Locate and identify every blood parasite.
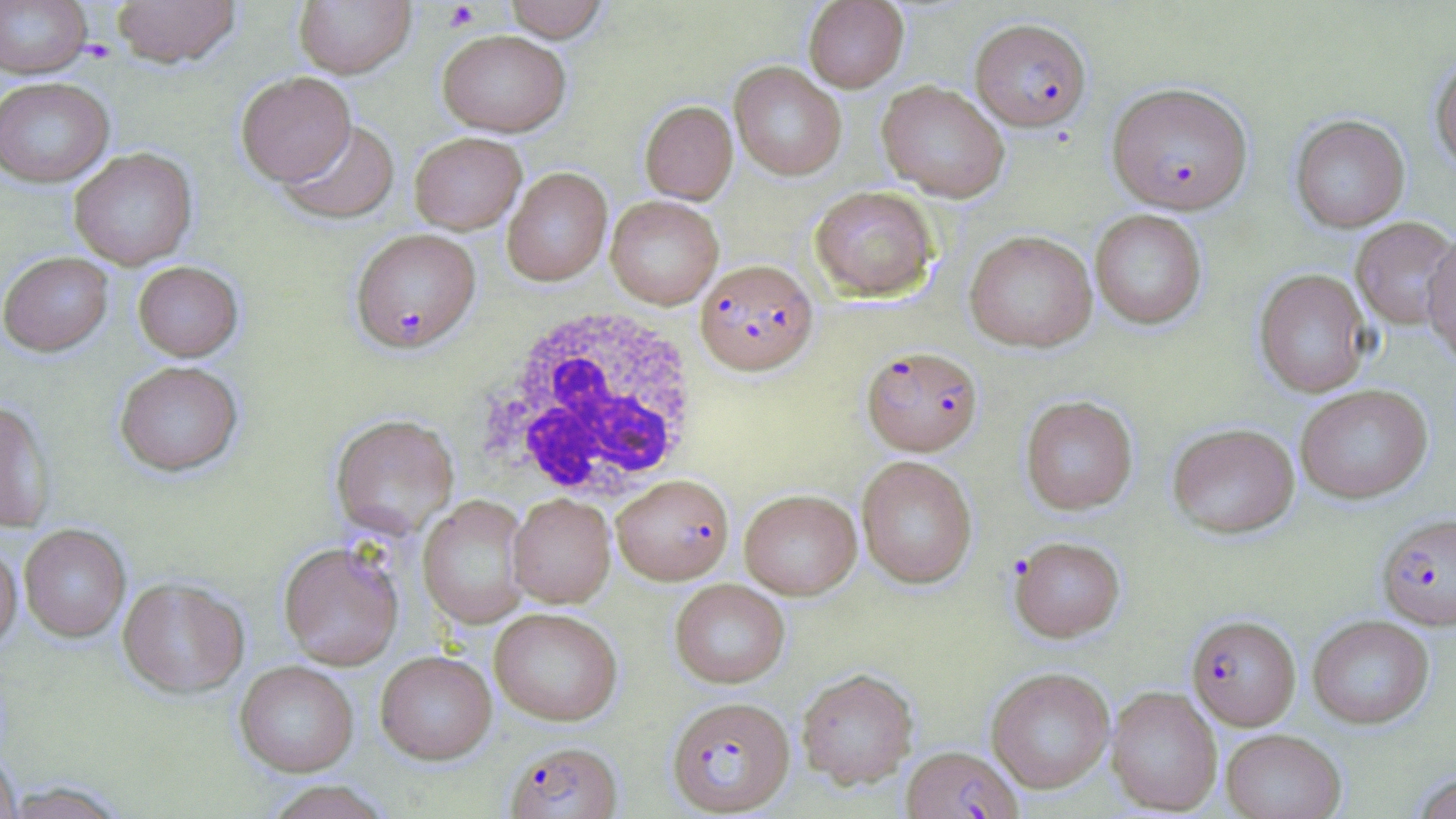
Approximate bounding boxes as (x1, y1, x2, y2) in pixels.
Plasmodium falciparum-infected red blood cells (subset): (970, 18, 1091, 132), (1107, 81, 1253, 215), (350, 228, 481, 353), (695, 259, 818, 375), (862, 346, 983, 456), (1377, 513, 1456, 630), (667, 696, 795, 815), (504, 740, 622, 819), (902, 745, 1021, 818).
No Plasmodium ovale, Plasmodium malariae, Plasmodium vivax, Babesia divergens, or Trypanosoma brucei observed.

Summary:
  - Uninfected red blood cell locations (subset): (0, 0, 93, 78), (111, 0, 242, 68), (293, 0, 415, 78), (502, 0, 610, 42), (803, 0, 909, 92), (437, 29, 572, 137), (1430, 53, 1456, 173), (729, 62, 846, 181), (236, 72, 356, 186), (0, 77, 115, 188), (876, 81, 1010, 202), (640, 100, 738, 203), (1290, 114, 1410, 233), (276, 118, 400, 224), (409, 132, 527, 234), (69, 147, 198, 269), (502, 167, 612, 286), (809, 185, 939, 301), (605, 195, 723, 309), (1090, 209, 1207, 330), (1351, 217, 1456, 329), (965, 230, 1097, 352), (1422, 230, 1456, 367), (0, 251, 114, 356), (132, 260, 243, 361), (1254, 268, 1372, 398), (114, 360, 242, 476), (1294, 384, 1433, 504), (1019, 395, 1138, 515), (0, 399, 55, 533), (331, 414, 459, 539), (1167, 422, 1300, 538), (856, 455, 977, 589), (740, 489, 861, 599), (508, 494, 615, 607), (418, 496, 530, 628), (19, 524, 131, 642), (1009, 535, 1126, 642), (0, 538, 22, 652), (278, 542, 404, 670), (117, 577, 249, 699), (670, 579, 790, 688), (489, 607, 623, 725), (1307, 614, 1435, 729), (375, 650, 497, 764), (234, 661, 359, 777), (986, 667, 1115, 794), (796, 668, 918, 788), (1105, 686, 1223, 815), (1221, 728, 1346, 818), (0, 749, 21, 819), (1408, 772, 1456, 819), (260, 780, 396, 819), (2, 782, 131, 818)
  - Platelet locations: (442, 2, 480, 32)
  - White blood cell locations: (478, 303, 703, 503)
  - Slide-level diagnosis: Plasmodium falciparum
  - Modality: optical microscopy
  - Magnification: 1000x
  - Field of view: single
  - Stain: May-Grünwald-Giemsa
  - Preparation: thin blood smear
  - Image size: 1456×819 pixels